Name the parasite shown.
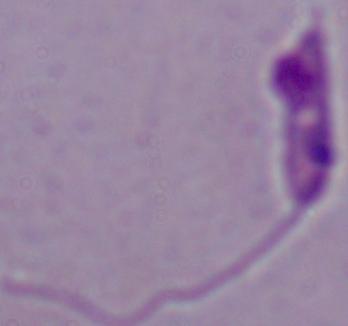

This is Leishmania.

modality: photomicrograph
magnification: 1000x